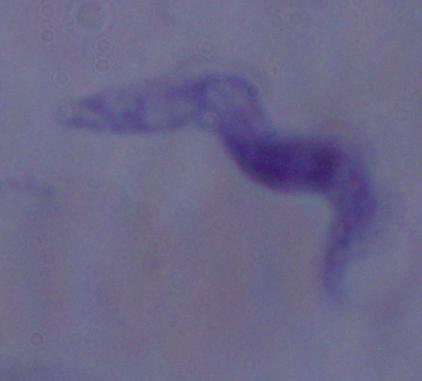

identification: trypanosome
modality: photomicrograph
magnification: 1000x